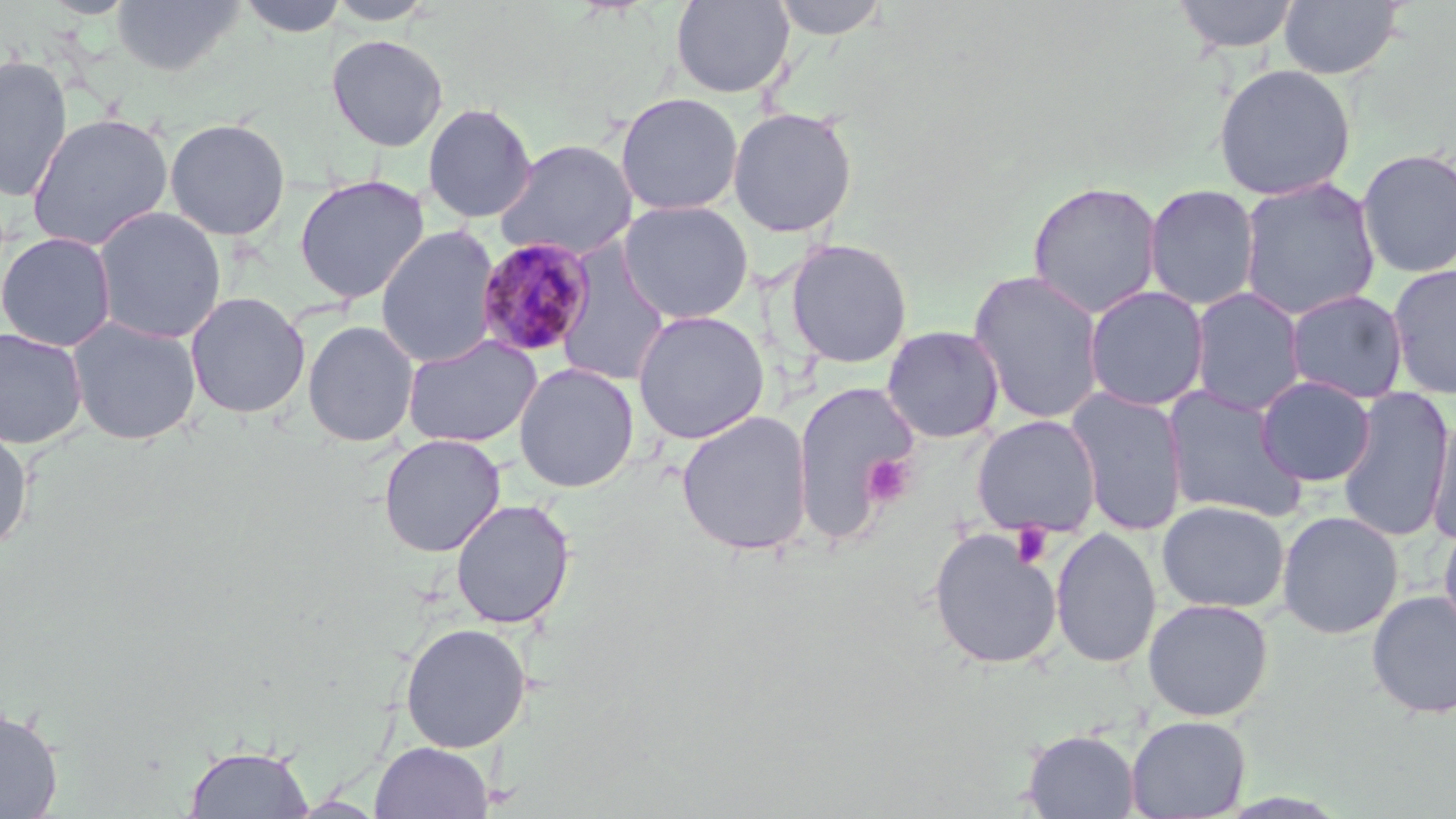

Approximate bounding boxes as (x1, y1, x2, y2) in pixels. Platelet locations: (862, 454, 914, 506), (1012, 523, 1055, 568). Plasmodium malariae-infected red blood cell locations: (474, 237, 596, 359). Uninfected red blood cell locations: (110, 0, 245, 77), (238, 0, 349, 38), (325, 0, 438, 26), (670, 0, 796, 98), (770, 0, 891, 40), (1172, 0, 1300, 53), (1278, 0, 1406, 80), (326, 33, 449, 152), (0, 55, 73, 203), (1212, 63, 1357, 200), (615, 92, 744, 216), (422, 102, 537, 223), (728, 107, 858, 237), (26, 112, 174, 252), (164, 117, 291, 241), (495, 138, 638, 261), (1355, 148, 1456, 279), (293, 174, 430, 304), (1238, 177, 1380, 321), (1026, 180, 1163, 318), (1144, 184, 1260, 311), (618, 200, 753, 324), (92, 206, 227, 344), (374, 225, 502, 369), (1, 231, 117, 352), (784, 238, 914, 368), (554, 242, 671, 388), (1386, 263, 1456, 400), (967, 270, 1106, 425), (1084, 285, 1209, 412), (1189, 287, 1307, 417), (1285, 289, 1409, 404), (185, 291, 310, 419), (631, 309, 770, 444), (66, 316, 202, 446), (302, 320, 419, 447), (881, 325, 1005, 444), (0, 327, 89, 449), (401, 334, 543, 448), (514, 362, 640, 493), (1255, 375, 1376, 487), (794, 381, 918, 543), (1162, 385, 1309, 523), (1065, 387, 1189, 536), (1337, 387, 1454, 543), (676, 411, 814, 557), (1425, 414, 1456, 546), (971, 415, 1102, 537), (0, 425, 33, 555), (378, 434, 506, 557), (449, 498, 576, 629), (1157, 500, 1290, 614), (1277, 511, 1404, 639), (1438, 518, 1456, 642), (1050, 526, 1162, 668), (928, 528, 1062, 670), (1366, 589, 1456, 720), (1143, 598, 1274, 721), (399, 622, 531, 753), (0, 706, 64, 817), (1126, 714, 1251, 818), (1022, 729, 1139, 818), (370, 741, 494, 819), (183, 745, 314, 818). Slide-level diagnosis: Plasmodium malariae. Image is 1456×819 pixels. Light microscopy. Thin blood smear. One field of a larger specimen. Captured at 1000x magnification. May-Grünwald-Giemsa stain.